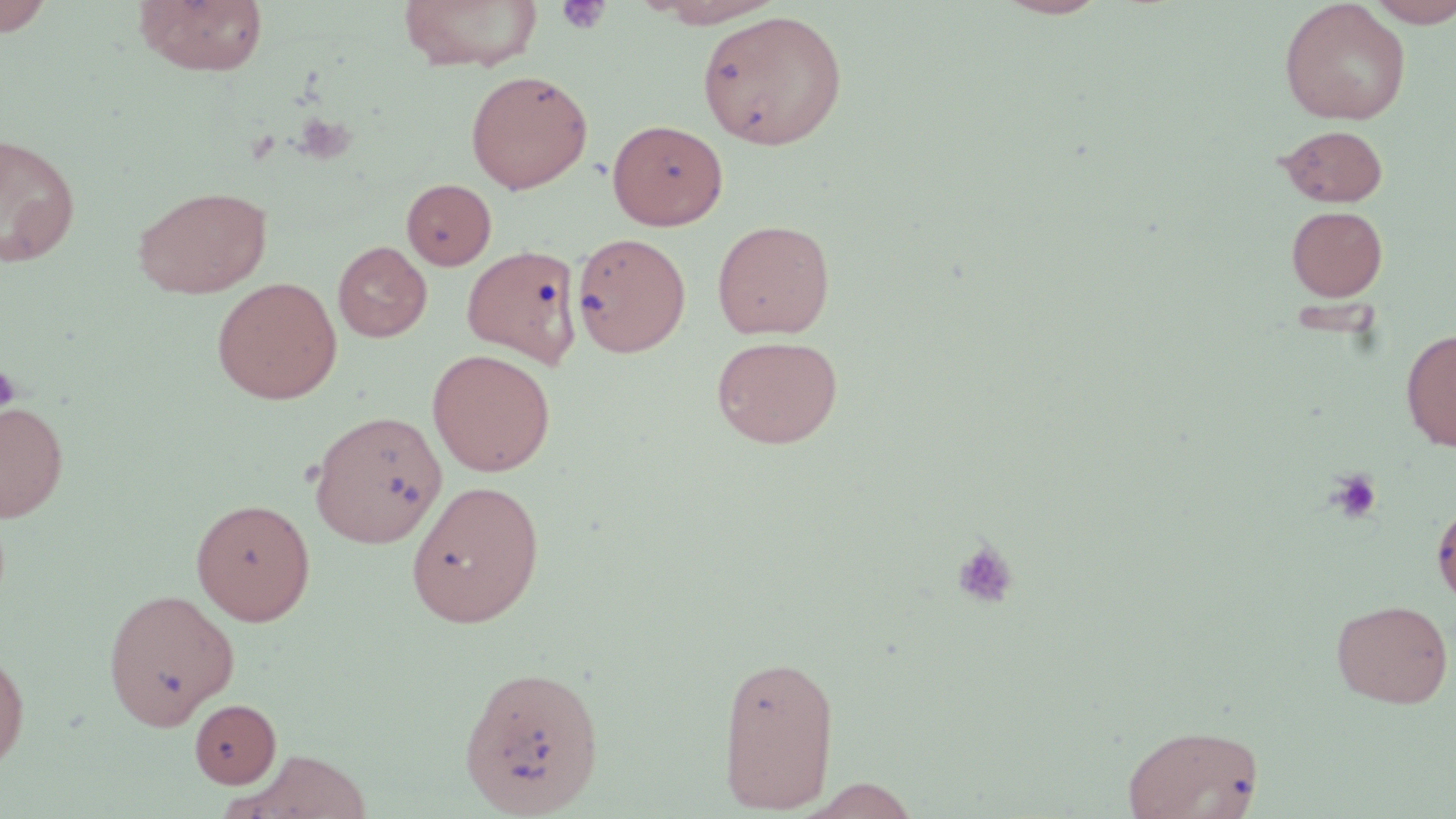
slide_level_diagnosis: no evidence of blood parasites
preparation: thin blood film
image_size: 1456×819 pixels
field_of_view: one of a larger specimen
platelet_locations: 'approximate bounding boxes as named x1/y1/x2/y2 corners in pixels: (x1=556, y1=1, x2=612, y2=35), (x1=291, y1=113, x2=357, y2=166), (x1=0, y1=365, x2=20, y2=415), (x1=1327, y1=469, x2=1383, y2=524), (x1=951, y1=538, x2=1020, y2=610)'
modality: optical microscopy
magnification: 1000x
uninfected_red_blood_cell_locations: 'approximate bounding boxes as named x1/y1/x2/y2 corners in pixels: (x1=0, y1=0, x2=57, y2=37), (x1=133, y1=0, x2=269, y2=76), (x1=398, y1=0, x2=544, y2=71), (x1=642, y1=0, x2=789, y2=27), (x1=993, y1=0, x2=1114, y2=19), (x1=1279, y1=0, x2=1412, y2=125), (x1=1365, y1=0, x2=1456, y2=27), (x1=697, y1=9, x2=848, y2=151), (x1=465, y1=69, x2=593, y2=194), (x1=607, y1=118, x2=728, y2=231), (x1=1277, y1=124, x2=1389, y2=208), (x1=0, y1=132, x2=81, y2=269), (x1=402, y1=178, x2=496, y2=270), (x1=132, y1=185, x2=273, y2=298), (x1=1286, y1=205, x2=1388, y2=301), (x1=712, y1=219, x2=835, y2=339), (x1=571, y1=231, x2=691, y2=357), (x1=333, y1=241, x2=431, y2=342), (x1=462, y1=244, x2=583, y2=368), (x1=211, y1=277, x2=342, y2=404), (x1=1401, y1=326, x2=1456, y2=452), (x1=710, y1=334, x2=844, y2=449), (x1=426, y1=349, x2=556, y2=476), (x1=0, y1=401, x2=69, y2=522), (x1=309, y1=410, x2=447, y2=547), (x1=406, y1=479, x2=545, y2=628), (x1=190, y1=498, x2=316, y2=625), (x1=1432, y1=499, x2=1456, y2=609), (x1=102, y1=587, x2=239, y2=729), (x1=1331, y1=598, x2=1454, y2=708), (x1=0, y1=644, x2=31, y2=774), (x1=717, y1=652, x2=840, y2=813), (x1=458, y1=663, x2=606, y2=817), (x1=190, y1=698, x2=281, y2=788), (x1=1122, y1=723, x2=1264, y2=818), (x1=232, y1=749, x2=373, y2=818), (x1=801, y1=778, x2=924, y2=818)'
stain: May-Grünwald-Giemsa